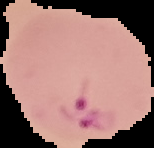
result = Plasmodium parasites identified
image size = 154×148 pixels
image type = segmented cell region on a black background
preparation = thin blood film